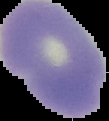
Summary:
  - Result: no Plasmodium parasites detected
  - Image type: segmented cell region on a black background
  - Image size: 109×121 pixels
  - Preparation: thin blood film